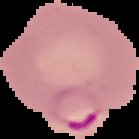
Summary:
  - Preparation: thin blood film
  - Result: malaria parasites identified
  - Image size: 139×139 pixels
  - Image type: segmented cell region with the area outside set to black